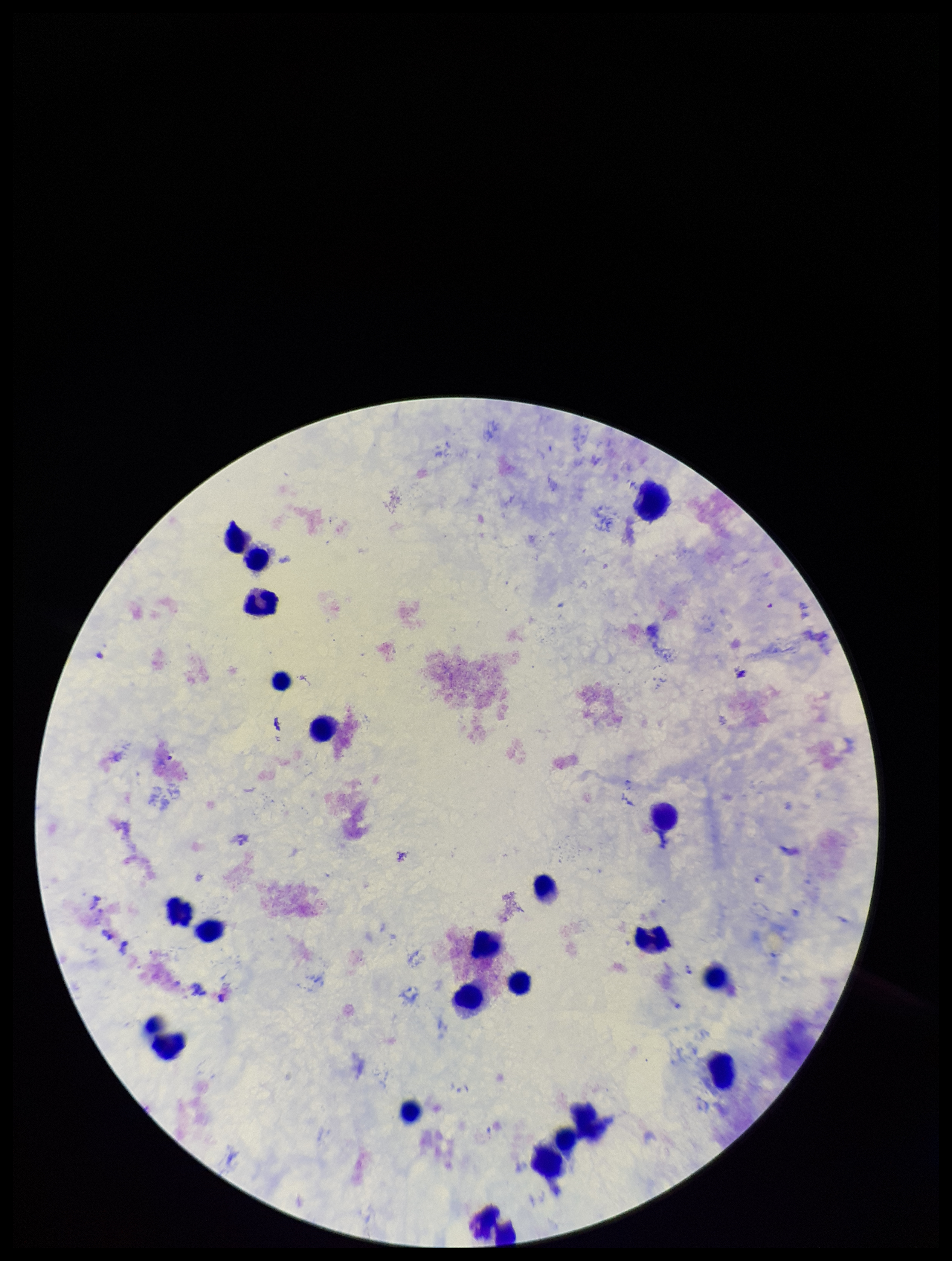
capture: smartphone photograph through the microscope eyepiece
patient_malaria_status: positive
preparation: thick smear
plasmodium_parasites: none identified
leukocyte_count: 21
stain: Giemsa
image_size: 952×1261 pixels
species_reported_for_this_patient: Plasmodium falciparum
parasite_count: 0
field_of_view: single